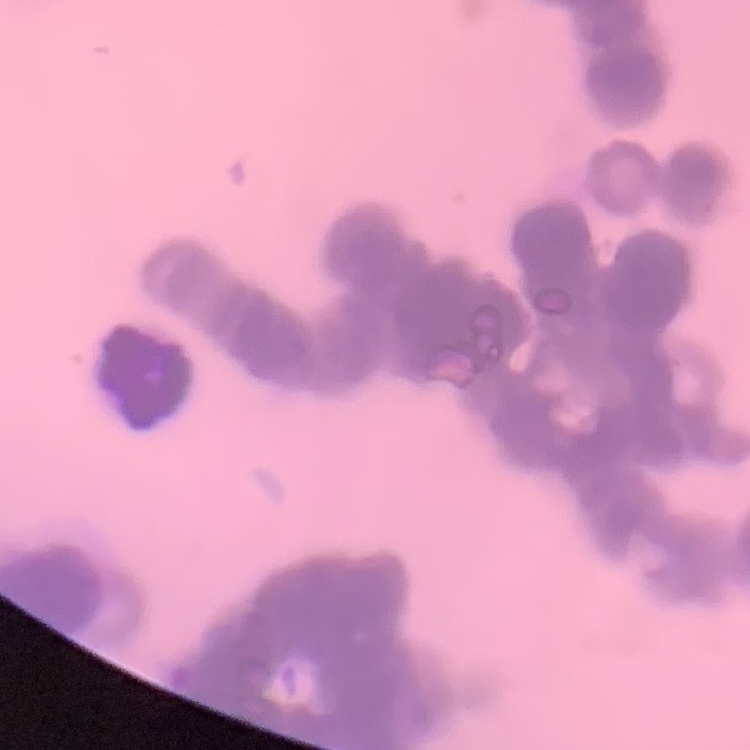
Summary:
  - Red blood cell morphology: rouleaux formation
  - Preparation: thin peripheral smear
  - Stain: Field's or Giemsa
  - Image type: one tile cut from a larger photomicrograph